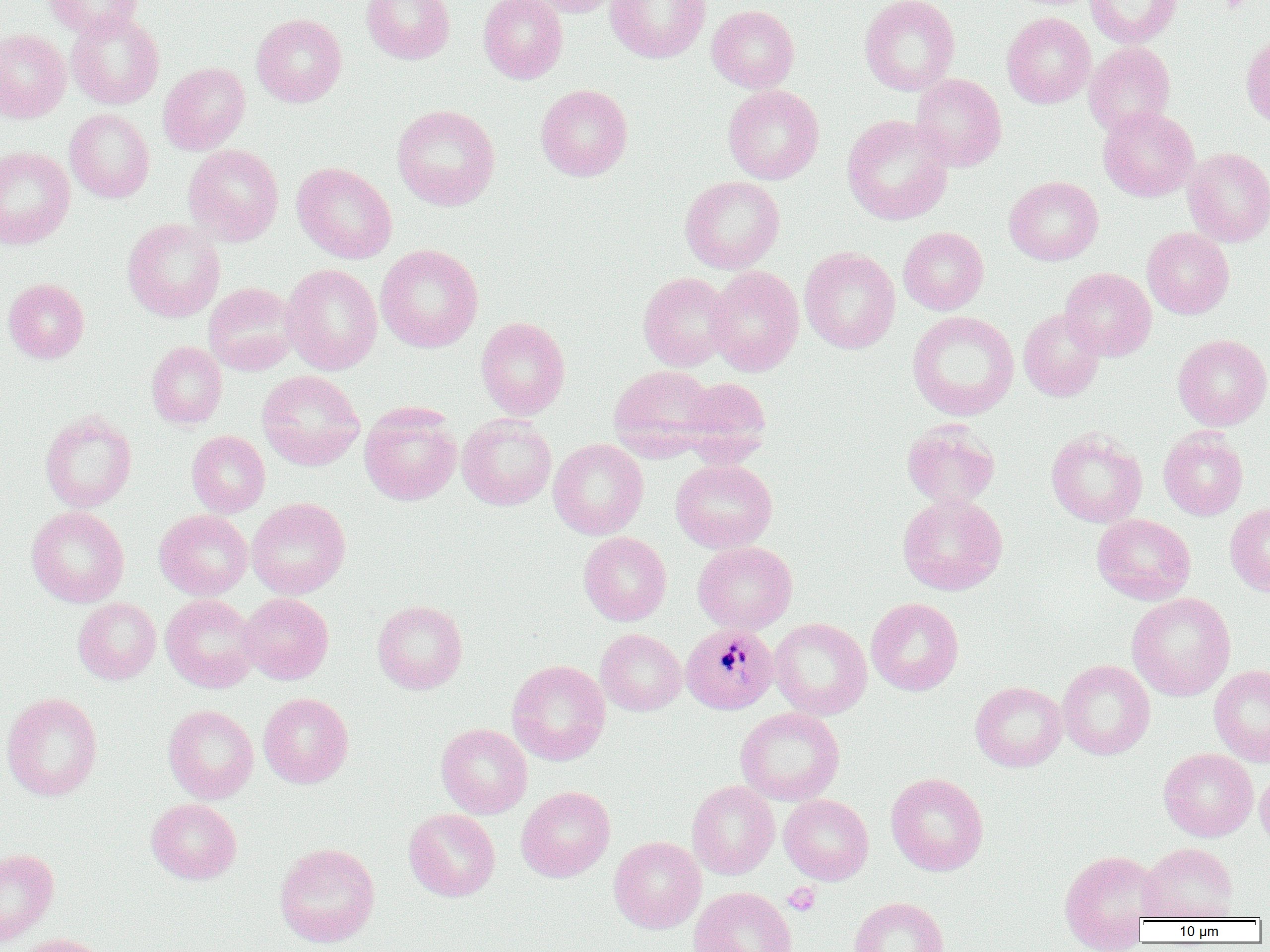

slide_level_diagnosis: Plasmodium malariae
field_of_view: single
platelet_locations: 'approximate bounding boxes as [x1, y1, x2, y2] in pixels: [783, 883, 821, 916]'
preparation: thin blood smear
uninfected_red_blood_cell_locations: 'approximate bounding boxes as [x1, y1, x2, y2] in pixels: [44, 0, 143, 38], [361, 0, 455, 65], [478, 0, 568, 84], [526, 0, 624, 17], [605, 0, 710, 63], [859, 0, 960, 95], [1085, 0, 1182, 48], [707, 5, 799, 93], [66, 11, 164, 109], [1002, 12, 1095, 108], [251, 13, 347, 107], [0, 29, 70, 122], [1241, 33, 1270, 127], [1084, 42, 1175, 137], [158, 62, 250, 154], [910, 74, 1007, 172], [535, 84, 632, 181], [723, 84, 824, 184], [392, 104, 500, 210], [1098, 107, 1199, 202], [65, 108, 154, 203], [842, 114, 953, 225], [183, 144, 284, 246], [0, 146, 75, 249], [1183, 147, 1270, 246], [292, 162, 397, 264], [680, 175, 785, 274], [1004, 176, 1103, 265], [123, 218, 225, 321], [898, 227, 989, 314], [1142, 227, 1234, 319], [375, 244, 484, 353], [799, 247, 900, 354], [281, 263, 382, 375], [705, 265, 804, 376], [1060, 267, 1156, 360], [638, 272, 735, 371], [3, 278, 89, 363], [204, 283, 299, 376], [1018, 308, 1105, 401], [907, 311, 1019, 420], [476, 316, 570, 420], [1172, 333, 1270, 430], [146, 341, 227, 429], [609, 363, 717, 458], [257, 370, 365, 471], [678, 377, 772, 461], [360, 402, 462, 505], [40, 410, 137, 512], [457, 414, 556, 511], [902, 419, 1000, 509], [1159, 427, 1248, 520], [1046, 428, 1147, 527], [186, 431, 270, 517], [548, 438, 648, 539], [671, 458, 777, 553], [897, 492, 1008, 595], [247, 497, 350, 599], [1225, 502, 1270, 597], [26, 506, 129, 607], [154, 509, 252, 600], [1092, 514, 1196, 605], [579, 532, 672, 625], [693, 541, 797, 634], [238, 592, 333, 684], [1127, 592, 1236, 701], [160, 594, 259, 693], [73, 597, 161, 684], [866, 597, 964, 696], [372, 599, 468, 694], [769, 617, 871, 719], [596, 628, 686, 715], [507, 659, 610, 765], [1057, 659, 1155, 759], [1209, 664, 1270, 766], [970, 680, 1067, 772], [1, 692, 103, 801], [258, 692, 354, 788], [163, 704, 259, 803], [735, 707, 845, 806], [436, 723, 532, 818], [1158, 748, 1258, 841], [1255, 766, 1270, 851], [886, 773, 988, 876], [687, 780, 779, 879], [516, 786, 615, 882], [779, 795, 874, 885], [146, 798, 241, 884], [404, 808, 500, 901], [609, 836, 706, 933], [274, 842, 380, 947], [1140, 842, 1239, 921], [0, 848, 58, 945], [1058, 850, 1163, 950], [688, 886, 798, 952], [849, 896, 949, 952], [11, 933, 112, 952]'
image_size: 1270×952 pixels
modality: optical microscopy
plasmodium_malariae_infected_red_blood_cell_locations: 'approximate bounding boxes as [x1, y1, x2, y2] in pixels: [680, 623, 778, 714]'
magnification: 1000x